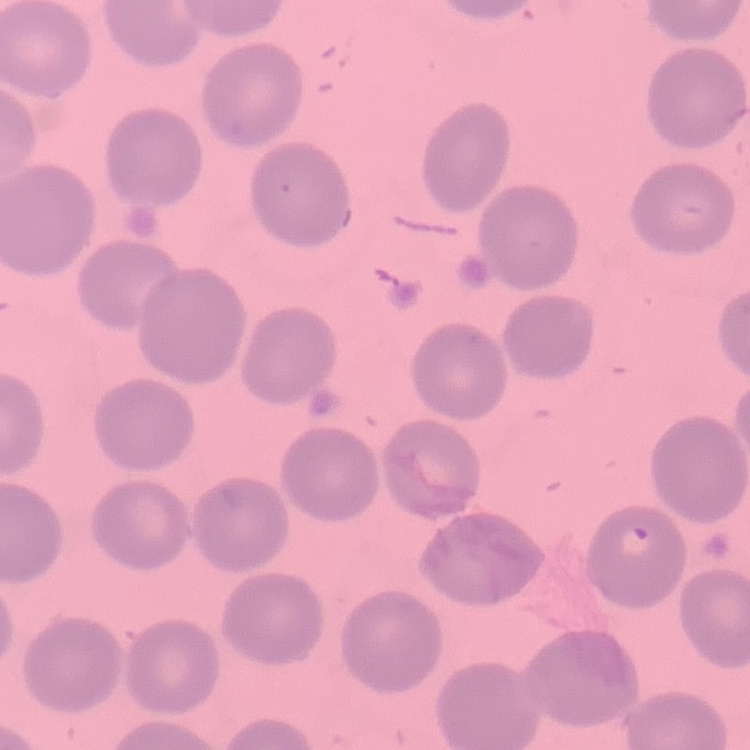

The erythrocytes show no rouleaux formation. Thin blood film. One tile cut from a larger photomicrograph. Stained with either Field's or Giemsa.